Assess the morphology of the red blood cells.
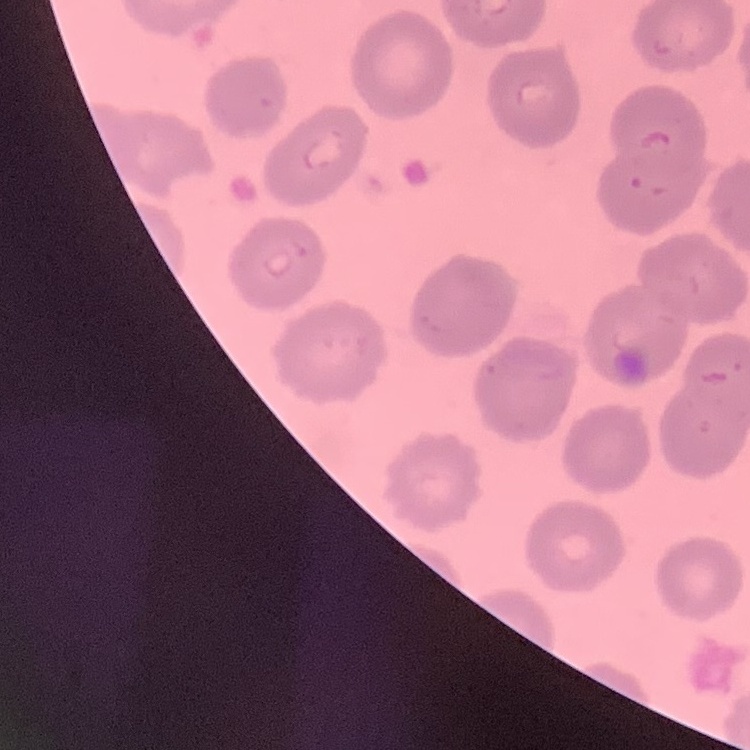
No rouleaux formation.

preparation = thin peripheral smear
stain = Field's or Giemsa
image type = square crop of a larger photomicrograph